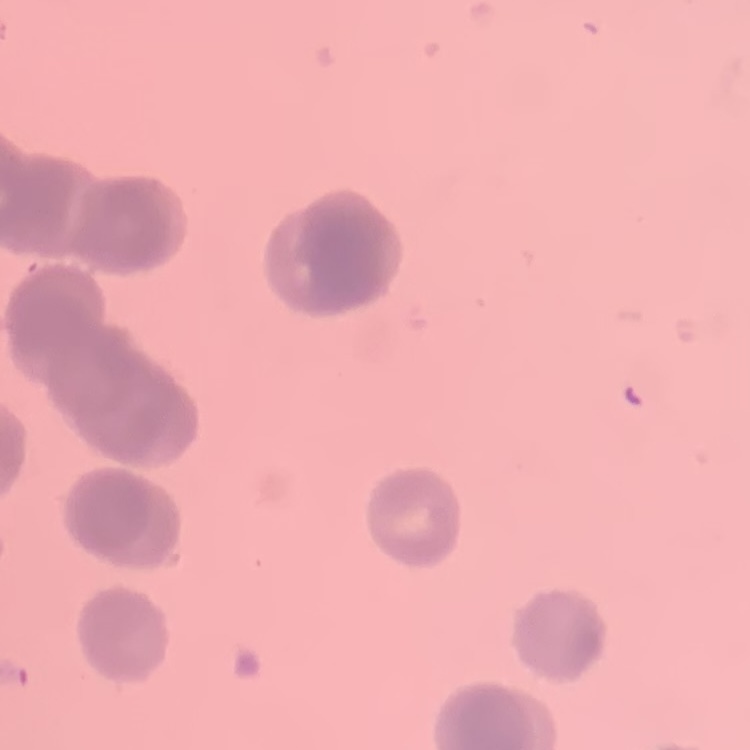

Summary:
  - Red blood cell morphology: rouleaux formation
  - Preparation: thin peripheral smear
  - Image type: square crop of a larger photomicrograph
  - Stain: Field's or Giemsa